Locate and identify every blood parasite.
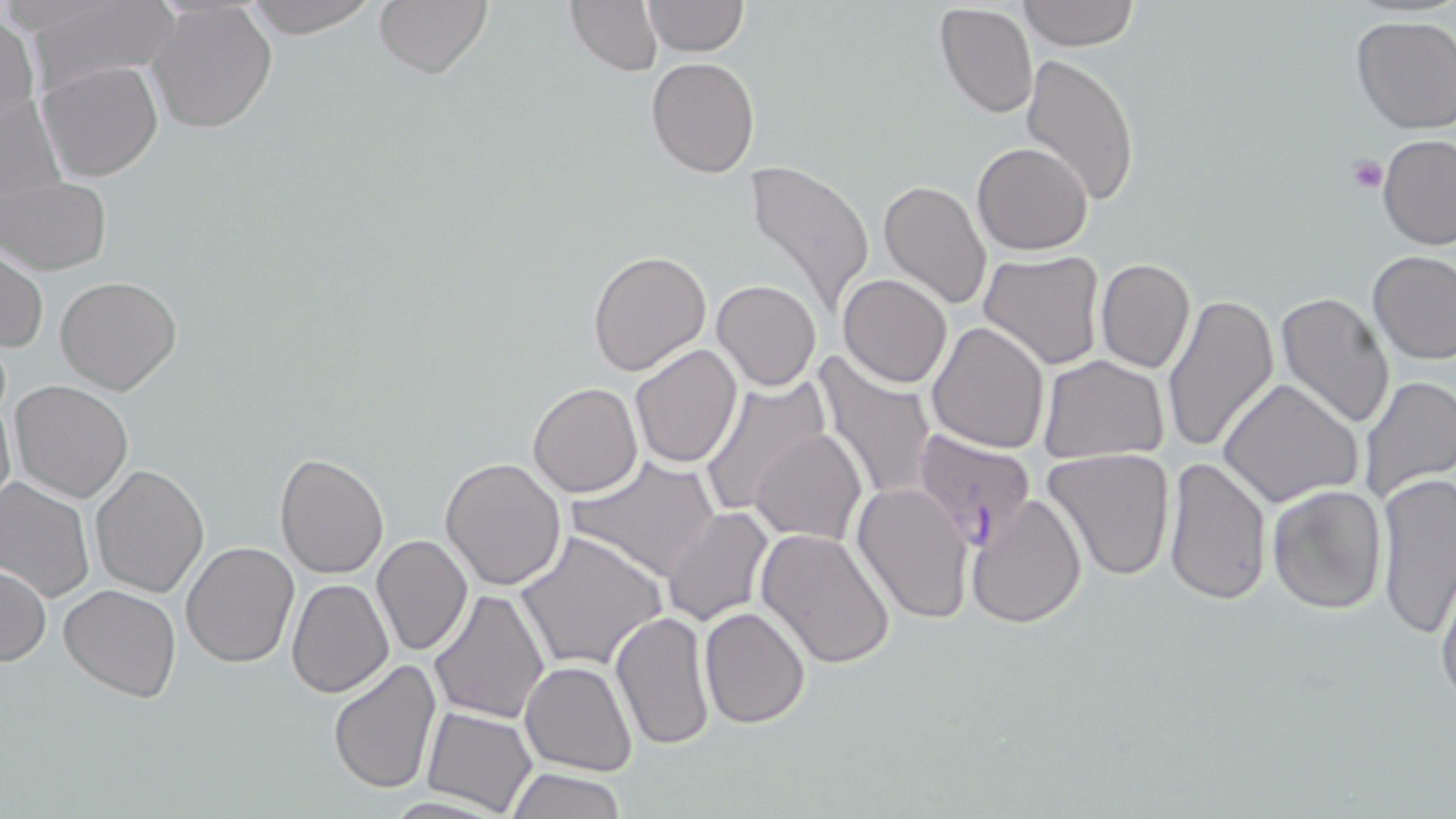

Approximate bounding boxes as (x1, y1, x2, y2) in pixels.
Plasmodium falciparum-infected red blood cells: (910, 428, 1038, 550).
No Plasmodium ovale, Plasmodium malariae, Plasmodium vivax, Babesia divergens, or Trypanosoma brucei observed.

Platelet locations: (1348, 157, 1387, 195). Uninfected red blood cell locations: (240, 0, 385, 37), (372, 0, 493, 79), (566, 0, 664, 75), (642, 0, 747, 56), (1018, 0, 1138, 50), (23, 1, 181, 98), (146, 1, 278, 134), (934, 1, 1038, 119), (1, 12, 40, 135), (1349, 15, 1455, 135), (1020, 52, 1141, 206), (646, 57, 759, 177), (38, 60, 165, 182), (1, 93, 66, 224), (1377, 134, 1456, 252), (973, 140, 1092, 254), (743, 159, 875, 318), (3, 176, 111, 275), (877, 179, 993, 311), (586, 248, 712, 376), (1, 249, 47, 354), (1366, 249, 1456, 366), (979, 251, 1105, 369), (1094, 258, 1195, 373), (54, 274, 183, 394), (838, 274, 952, 388), (712, 279, 821, 391), (1162, 292, 1280, 454), (1274, 292, 1396, 432), (927, 321, 1049, 452), (629, 343, 743, 467), (813, 354, 939, 507), (1037, 355, 1169, 463), (1356, 375, 1455, 504), (698, 376, 830, 518), (1218, 378, 1363, 508), (8, 381, 134, 503), (529, 383, 643, 498), (0, 393, 15, 519), (751, 429, 867, 546), (1043, 447, 1176, 581), (274, 452, 389, 579), (567, 455, 721, 583), (1162, 456, 1272, 605), (441, 458, 568, 592), (89, 463, 210, 596), (1373, 470, 1456, 635), (0, 476, 97, 602), (1266, 483, 1388, 614), (852, 484, 975, 623), (966, 494, 1088, 630), (662, 507, 773, 626), (754, 526, 897, 670), (514, 528, 669, 671), (372, 535, 472, 657), (181, 541, 301, 668), (1, 563, 49, 667), (1434, 569, 1456, 712), (286, 577, 393, 697), (59, 584, 182, 701), (430, 588, 549, 724), (699, 606, 811, 730), (610, 609, 716, 750), (327, 659, 442, 796), (519, 661, 636, 776), (423, 707, 537, 816), (503, 766, 629, 819). Slide-level diagnosis: Plasmodium falciparum. Image is 1456×819 pixels. May-Grünwald-Giemsa stain. Optical microscopy. Thin blood film. Captured at 1000x magnification. Single field of view.